Give the position of every Plasmodium parasite visible.
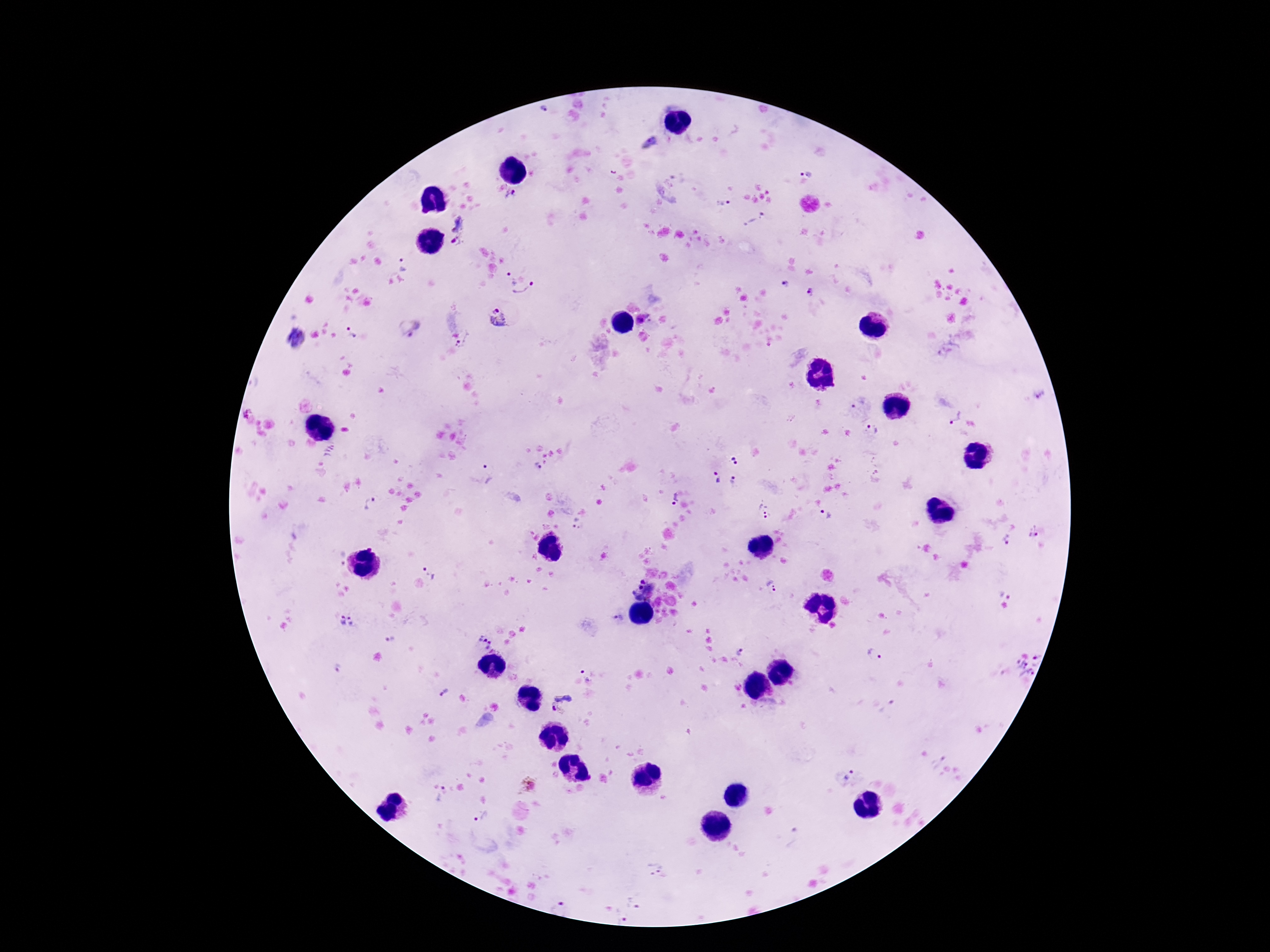
Approximate centers as [x, y] in pixels.
Plasmodium parasites: [649, 142], [806, 169], [513, 197], [722, 203], [755, 219], [461, 222], [456, 243], [402, 264], [508, 279], [784, 285], [524, 290], [810, 294], [501, 318], [413, 327], [352, 334], [295, 340], [464, 341], [246, 414], [953, 417], [872, 431], [734, 461], [536, 468], [489, 473], [715, 478], [734, 481], [673, 500], [369, 503], [765, 510], [826, 514], [573, 522], [1034, 533], [1007, 540], [340, 558], [430, 571], [773, 587], [643, 588], [1006, 595], [336, 620], [354, 620], [617, 620], [393, 640], [485, 641], [742, 651], [876, 654], [335, 667], [1026, 668], [587, 675], [445, 691], [564, 704], [936, 761], [847, 772], [441, 794], [481, 817], [793, 837], [653, 868], [636, 900], [560, 906], [615, 915].

Summary:
  - Preparation: thick blood smear
  - Field of view: single
  - Image size: 1270×952 pixels
  - Patient malaria status: positive
  - Stain: Giemsa
  - Magnification: 100x
  - Capture: smartphone camera through the microscope eyepiece